Locate every Plasmodium parasite.
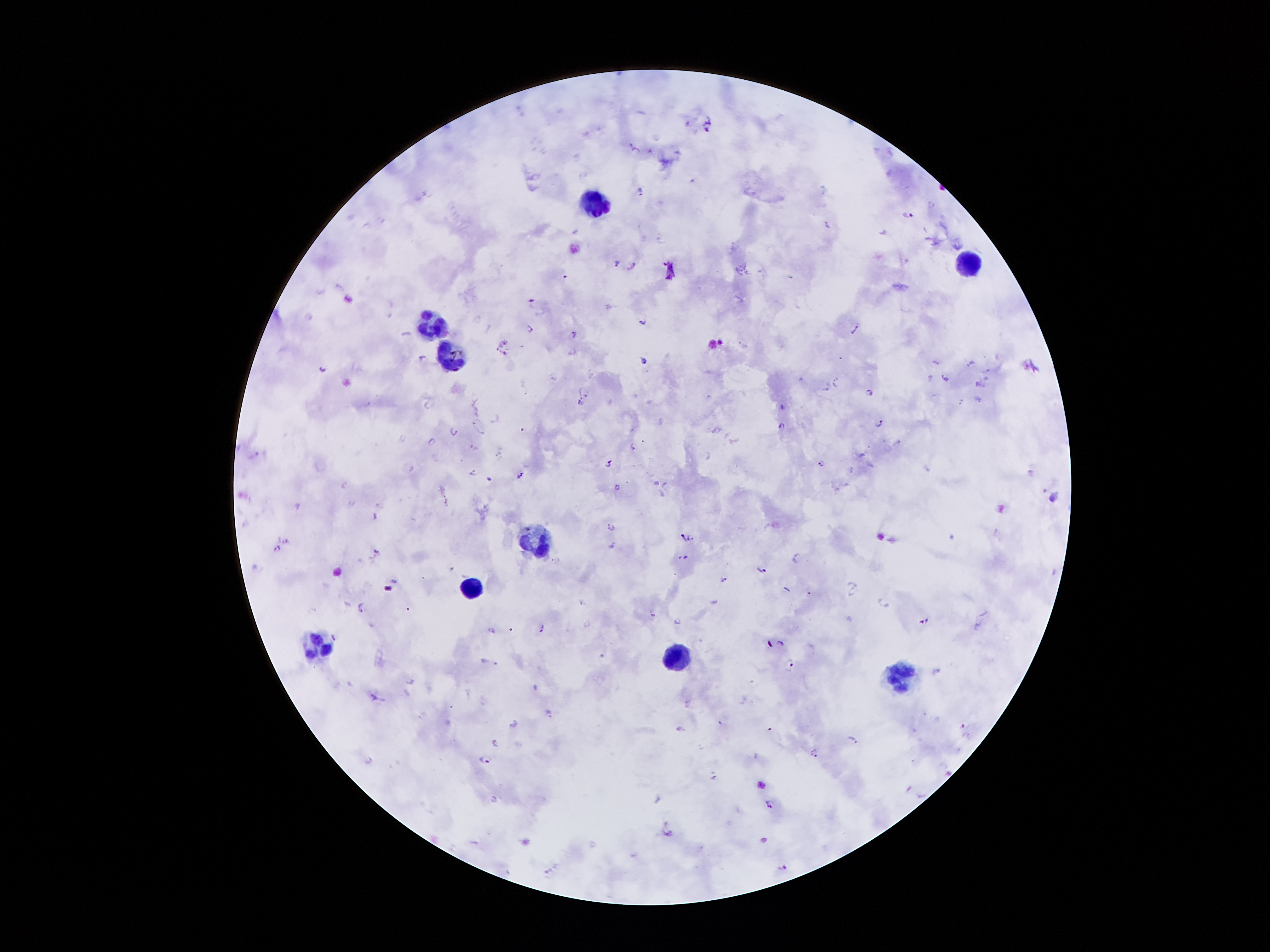
Approximate object centers, in pixels from the top-left corner.
Plasmodium parasites: (x=687, y=123), (x=707, y=128), (x=633, y=147), (x=692, y=181), (x=640, y=192), (x=933, y=205), (x=911, y=215), (x=827, y=223), (x=616, y=261), (x=632, y=265), (x=564, y=276), (x=531, y=299), (x=307, y=316), (x=639, y=320), (x=855, y=326), (x=528, y=327), (x=531, y=327), (x=572, y=333), (x=401, y=334), (x=573, y=353), (x=421, y=357), (x=643, y=360), (x=934, y=361), (x=969, y=362), (x=321, y=367), (x=943, y=376), (x=551, y=377), (x=836, y=380), (x=929, y=380), (x=826, y=388), (x=867, y=390), (x=586, y=395), (x=978, y=398), (x=578, y=401), (x=961, y=402), (x=425, y=406), (x=781, y=407), (x=493, y=420), (x=880, y=421), (x=472, y=422), (x=474, y=422), (x=780, y=426), (x=713, y=430), (x=454, y=431), (x=482, y=433), (x=429, y=440), (x=898, y=441), (x=472, y=446), (x=632, y=447), (x=255, y=451), (x=861, y=453), (x=498, y=454), (x=609, y=461), (x=819, y=461), (x=850, y=470), (x=474, y=471), (x=520, y=474), (x=489, y=479), (x=343, y=481), (x=653, y=482), (x=617, y=486), (x=1051, y=499), (x=445, y=501), (x=373, y=518), (x=611, y=526), (x=680, y=536), (x=691, y=537), (x=287, y=539), (x=610, y=543), (x=275, y=547), (x=375, y=549), (x=684, y=556), (x=797, y=556), (x=761, y=568), (x=724, y=578), (x=394, y=579), (x=855, y=584), (x=807, y=592), (x=849, y=595), (x=715, y=601), (x=580, y=603), (x=887, y=605), (x=360, y=609), (x=651, y=612), (x=675, y=622), (x=921, y=622), (x=585, y=624), (x=541, y=627), (x=491, y=630), (x=334, y=636), (x=779, y=641), (x=483, y=660), (x=790, y=663), (x=495, y=664), (x=938, y=670), (x=536, y=686), (x=373, y=696), (x=686, y=702), (x=548, y=711), (x=513, y=723), (x=719, y=723), (x=962, y=724), (x=679, y=728), (x=853, y=740), (x=493, y=742), (x=814, y=753), (x=486, y=758), (x=369, y=760), (x=712, y=775), (x=920, y=794), (x=658, y=798), (x=493, y=800), (x=768, y=804), (x=666, y=832), (x=782, y=866), (x=545, y=871).

Leukocyte locations: (x=598, y=203), (x=969, y=262), (x=432, y=323), (x=450, y=356), (x=538, y=541), (x=468, y=587), (x=316, y=644), (x=674, y=657), (x=896, y=676). Photographed through the microscope eyepiece with a smartphone camera. Patient malaria status: positive for Plasmodium falciparum. Thick blood film. Image is 1270×952 pixels. Single field of view. 100x magnification. Giemsa stain.